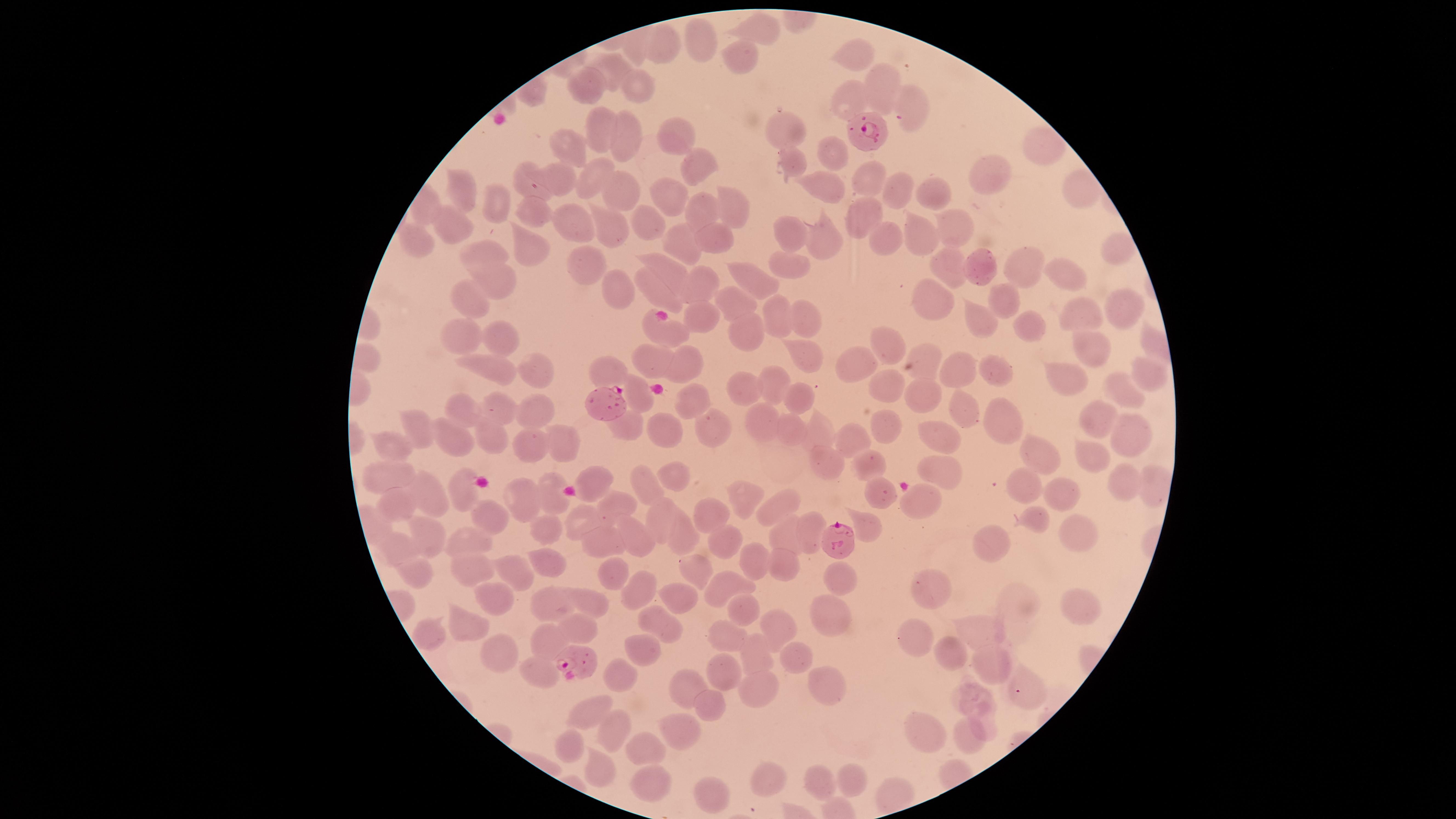
parasitized red blood cells = approximate marker points as {x, y} in pixels: {865, 127}, {606, 403}, {840, 542}, {582, 657}
uninfected red blood cells = approximate marker points as {x, y} in pixels: {762, 29}, {706, 39}, {671, 42}, {858, 54}, {737, 60}, {615, 70}, {642, 85}, {876, 87}, {589, 88}, {851, 101}, {902, 110}, {784, 124}, {601, 129}, {670, 135}, {624, 138}, {571, 147}, {1044, 148}, {832, 154}, {789, 160}, {697, 168}, {991, 173}, {529, 175}, {563, 178}, {871, 179}, {821, 181}, {597, 182}, {624, 188}, {895, 189}, {937, 189}, {1075, 189}, {466, 191}, {665, 191}, {730, 202}, {500, 206}, {701, 210}, {539, 212}, {648, 216}, {864, 216}, {448, 225}, {572, 225}, {616, 226}, {952, 227}, {917, 231}, {794, 233}, {883, 235}, {711, 237}, {831, 239}, {414, 240}, {681, 244}, {532, 247}, {481, 253}, {1121, 255}, {796, 263}, {585, 264}, {947, 265}, {985, 268}, {1020, 268}, {672, 269}, {1071, 270}, {747, 277}, {498, 282}, {702, 284}, {617, 293}, {657, 293}, {1002, 295}, {733, 299}, {927, 302}, {469, 304}, {977, 306}, {1128, 310}, {1086, 314}, {779, 317}, {702, 318}, {802, 320}, {1023, 320}, {743, 327}, {665, 333}, {461, 335}, {503, 341}, {887, 342}, {1089, 347}, {812, 352}, {929, 354}, {653, 359}, {690, 363}, {860, 364}, {495, 369}, {612, 370}, {955, 370}, {986, 370}, {539, 374}, {1062, 375}, {1156, 379}, {776, 386}, {890, 386}, {635, 388}, {745, 388}, {921, 390}, {1125, 392}, {800, 397}, {691, 401}, {964, 403}, {534, 409}, {496, 410}, {465, 412}, {1000, 414}, {1095, 414}, {762, 423}, {631, 424}, {422, 425}, {711, 425}, {792, 428}, {819, 428}, {669, 429}, {889, 429}, {937, 434}, {1125, 435}, {496, 436}, {450, 437}, {852, 437}, {393, 444}, {565, 445}, {531, 446}, {1031, 449}, {1091, 452}, {826, 465}, {865, 466}, {594, 471}, {942, 471}, {671, 472}, {1120, 474}, {384, 476}, {640, 483}, {1018, 483}, {1151, 484}, {878, 488}, {427, 490}, {462, 490}, {1056, 492}, {748, 495}, {526, 498}, {918, 502}, {393, 503}, {613, 505}, {776, 508}, {656, 515}, {712, 515}, {490, 516}, {1030, 517}, {579, 523}, {815, 524}, {870, 527}, {425, 530}, {547, 532}, {639, 533}, {678, 534}, {785, 534}, {1072, 537}, {472, 540}, {987, 543}, {596, 544}, {725, 544}, {399, 552}, {546, 560}, {753, 562}, {783, 565}, {470, 567}, {616, 570}, {698, 571}, {519, 572}, {844, 577}, {416, 579}, {720, 586}, {640, 587}, {931, 588}, {491, 596}, {680, 597}, {547, 602}, {593, 602}, {1084, 603}, {747, 610}, {828, 616}, {660, 622}, {776, 623}, {470, 625}, {582, 631}, {428, 633}, {983, 634}, {727, 635}, {918, 638}, {546, 640}, {644, 645}, {950, 650}, {499, 654}, {756, 658}, {801, 661}, {997, 666}, {720, 668}, {542, 677}, {624, 677}, {765, 687}, {691, 688}, {1021, 691}, {824, 694}, {967, 698}, {710, 707}, {593, 712}, {612, 731}, {926, 732}, {668, 734}, {965, 735}, {571, 747}, {641, 747}, {601, 773}, {855, 775}, {768, 776}, {646, 778}, {816, 782}, {708, 793}
stain = Giemsa
species = Plasmodium falciparum
field of view = single
image size = 1456×819 pixels
preparation = thin blood smear
visible region = circular
capture = smartphone photograph through the microscope eyepiece
presence = malaria parasites seen